Report the malaria status of this cell.
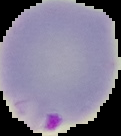

It is parasitized.

preparation = thin blood smear
image type = segmented cell region with the area outside set to black
image size = 121×136 pixels